Assess this cell for malaria.
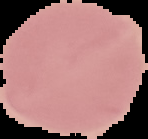
It is uninfected.

The area outside the segmented cell region is set to black. Image is 148×139 pixels. From a thin blood film.